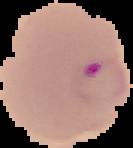

Image is 133×148 pixels. Segmented cell region on a black background. From a thin blood smear. Malaria status: parasitized.